Assess this cell for malaria.
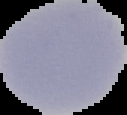
Uninfected.

The area outside the segmented cell region is set to black. Image is 127×115 pixels. From a thin blood smear.